Outline each Plasmodium falciparum-infected red blood cell.
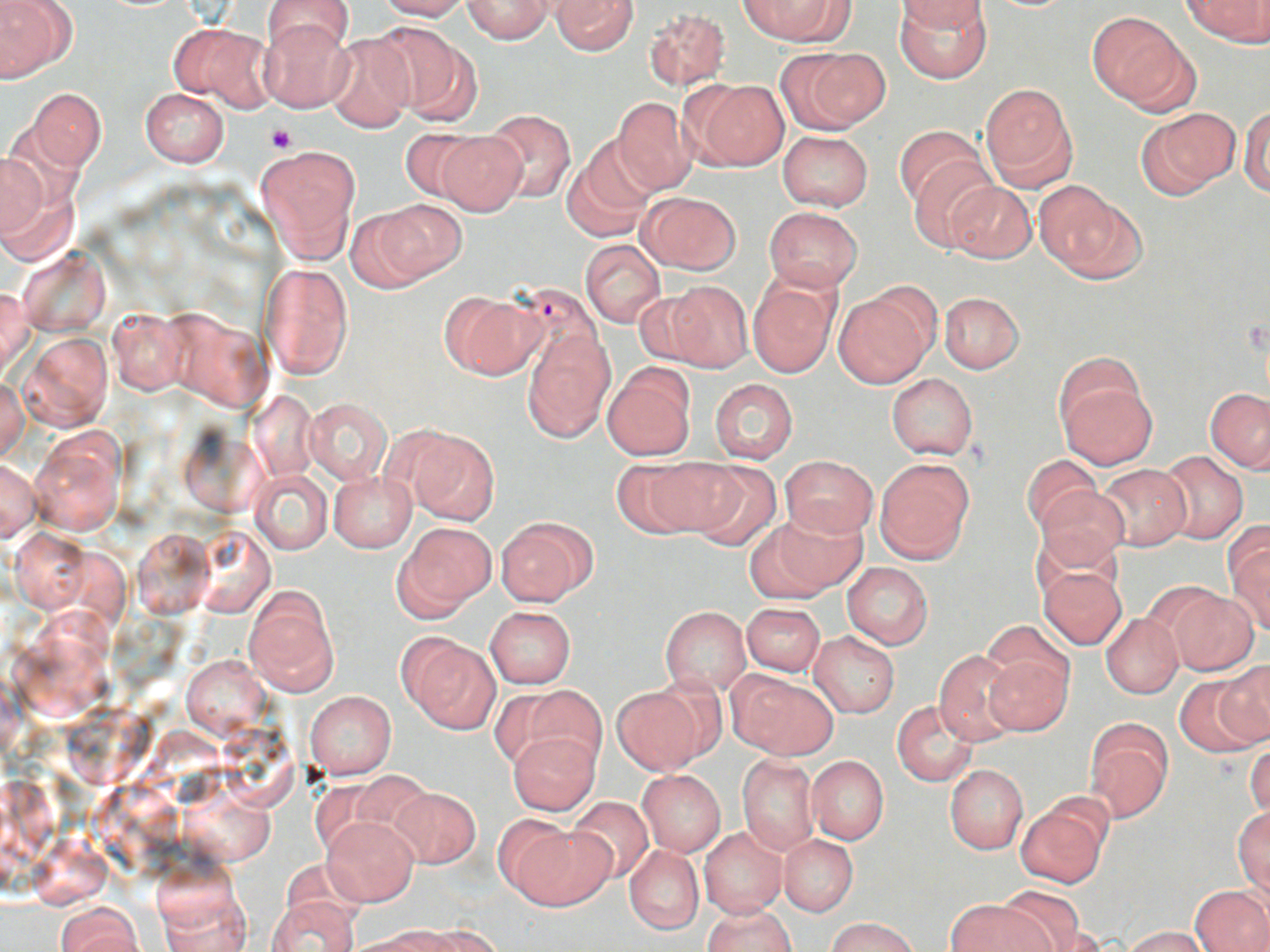

Approximate bounding boxes as (x1,y1)-(x2,y2) corner pairs in pixels.
Plasmodium falciparum-infected red blood cells: (505,281)-(606,378).

Summary:
  - Uninfected red blood cell locations: (373,0)-(472,21), (461,0)-(553,43), (549,0)-(638,56), (738,0)-(847,43), (896,0)-(990,32), (1183,0)-(1269,45), (0,1)-(75,81), (261,1)-(354,58), (894,4)-(993,84), (642,6)-(731,90), (1086,11)-(1192,109), (258,17)-(353,112), (375,20)-(481,124), (171,22)-(270,108), (322,33)-(416,132), (783,45)-(888,133), (683,78)-(790,171), (979,83)-(1077,189), (140,88)-(229,168), (29,89)-(106,170), (612,97)-(696,195), (1135,107)-(1240,200), (1240,107)-(1270,197), (482,110)-(576,201), (895,124)-(984,210), (399,126)-(489,203), (433,131)-(528,216), (778,131)-(873,210), (563,142)-(654,240), (255,143)-(358,261), (0,150)-(49,244), (907,155)-(997,247), (0,162)-(79,267), (945,181)-(1036,264), (1038,184)-(1146,282), (638,190)-(741,274), (365,198)-(465,285), (763,206)-(863,292), (581,241)-(665,327), (19,249)-(109,334), (258,262)-(353,378), (748,273)-(840,378), (663,279)-(753,371), (1,284)-(35,377), (834,288)-(936,386), (439,291)-(543,380), (634,292)-(713,367), (940,292)-(1024,374), (108,310)-(189,394), (522,331)-(614,441), (21,332)-(112,430), (603,364)-(695,459), (1055,367)-(1157,468), (888,373)-(977,460), (708,377)-(798,465), (0,378)-(28,460), (1205,388)-(1270,472), (249,389)-(317,480), (304,397)-(391,483), (398,426)-(500,525), (29,429)-(126,536), (1157,451)-(1248,544), (1023,454)-(1100,535), (781,456)-(877,538), (619,457)-(732,538), (1,459)-(39,541), (875,459)-(973,562), (680,462)-(783,551), (1098,465)-(1191,549), (251,469)-(332,554), (328,471)-(416,551), (1036,485)-(1128,570), (773,506)-(868,593), (495,516)-(596,605), (742,521)-(841,603), (398,523)-(496,614), (133,527)-(213,620), (11,528)-(90,611), (1224,528)-(1270,628), (841,563)-(933,648), (1039,567)-(1126,649), (243,583)-(339,697), (1160,588)-(1258,675), (740,601)-(826,676), (485,606)-(575,688), (659,606)-(750,695), (1100,613)-(1183,699), (983,620)-(1074,701), (809,631)-(900,718), (402,636)-(500,733), (983,649)-(1071,736), (932,651)-(1021,746), (180,654)-(270,739), (1212,661)-(1270,747), (729,672)-(838,760), (1175,678)-(1260,758), (517,685)-(605,772), (611,685)-(710,774), (305,690)-(397,779), (892,699)-(979,786), (1083,721)-(1171,823), (507,732)-(599,814), (1246,740)-(1270,819), (737,755)-(818,854), (808,755)-(889,844), (945,764)-(1028,854), (638,770)-(725,856), (388,786)-(480,866), (568,796)-(654,884), (1015,801)-(1108,889), (1234,806)-(1269,897), (323,816)-(418,904), (510,819)-(613,911), (699,828)-(787,918), (779,835)-(857,916), (625,844)-(703,933), (153,868)-(252,952), (1190,886)-(1270,952), (998,887)-(1087,949), (267,897)-(361,952), (947,899)-(1048,952), (55,901)-(142,951), (702,904)-(796,952), (828,917)-(917,952), (415,922)-(503,951), (1124,926)-(1208,951), (337,932)-(441,952)
  - Platelet locations: (267,124)-(296,153)
  - Slide-level diagnosis: Plasmodium falciparum
  - Magnification: 1000x
  - Image size: 1270×952 pixels
  - Stain: May-Grünwald-Giemsa
  - Field of view: single
  - Preparation: thin blood smear
  - Modality: light microscopy